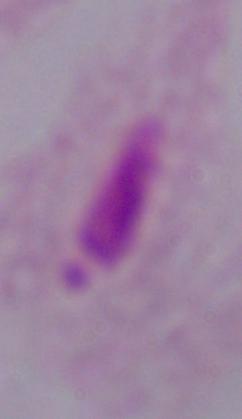
identification = trichomonad
magnification = 1000x
modality = photomicrograph